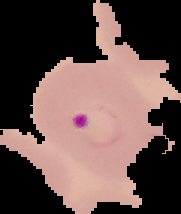 Segmented cell region on a black background. From a thin blood smear. Image is 181×214 pixels. Result: Plasmodium parasites identified.